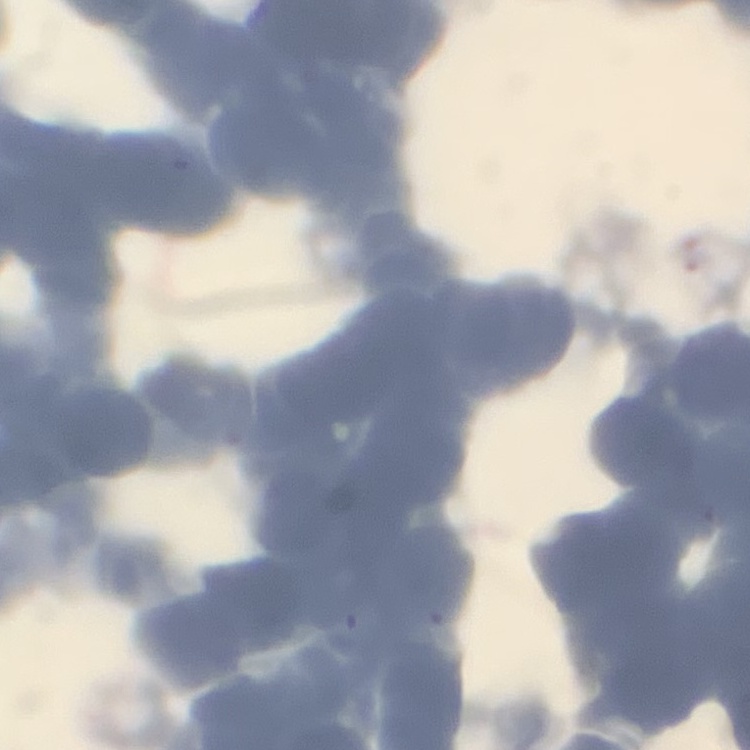
Summary:
  - Red blood cell morphology: rouleaux formation
  - Image type: one tile cut from a larger photomicrograph
  - Stain: Field's or Giemsa
  - Preparation: thin blood smear